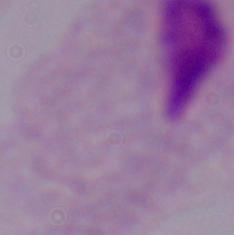

A trichomonad is seen. Micrograph. 1000x magnification.